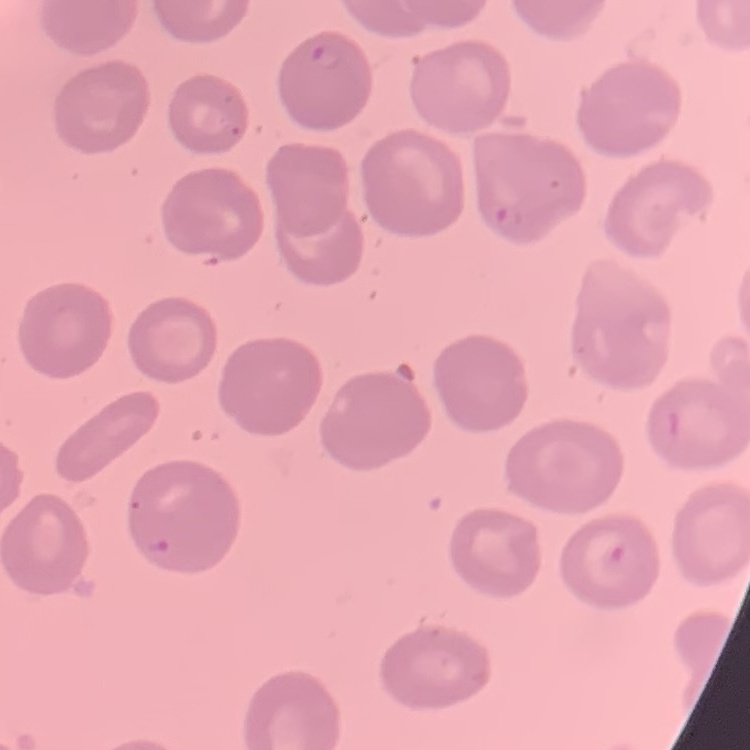
erythrocyte morphology = no rouleaux formation
stain = Field's or Giemsa
preparation = thin blood film
image type = square crop of a larger photomicrograph